State which parasite is depicted.
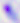

Toxoplasma gondii.

Captured at 400x magnification. Photomicrograph.